State the blood parasite species.
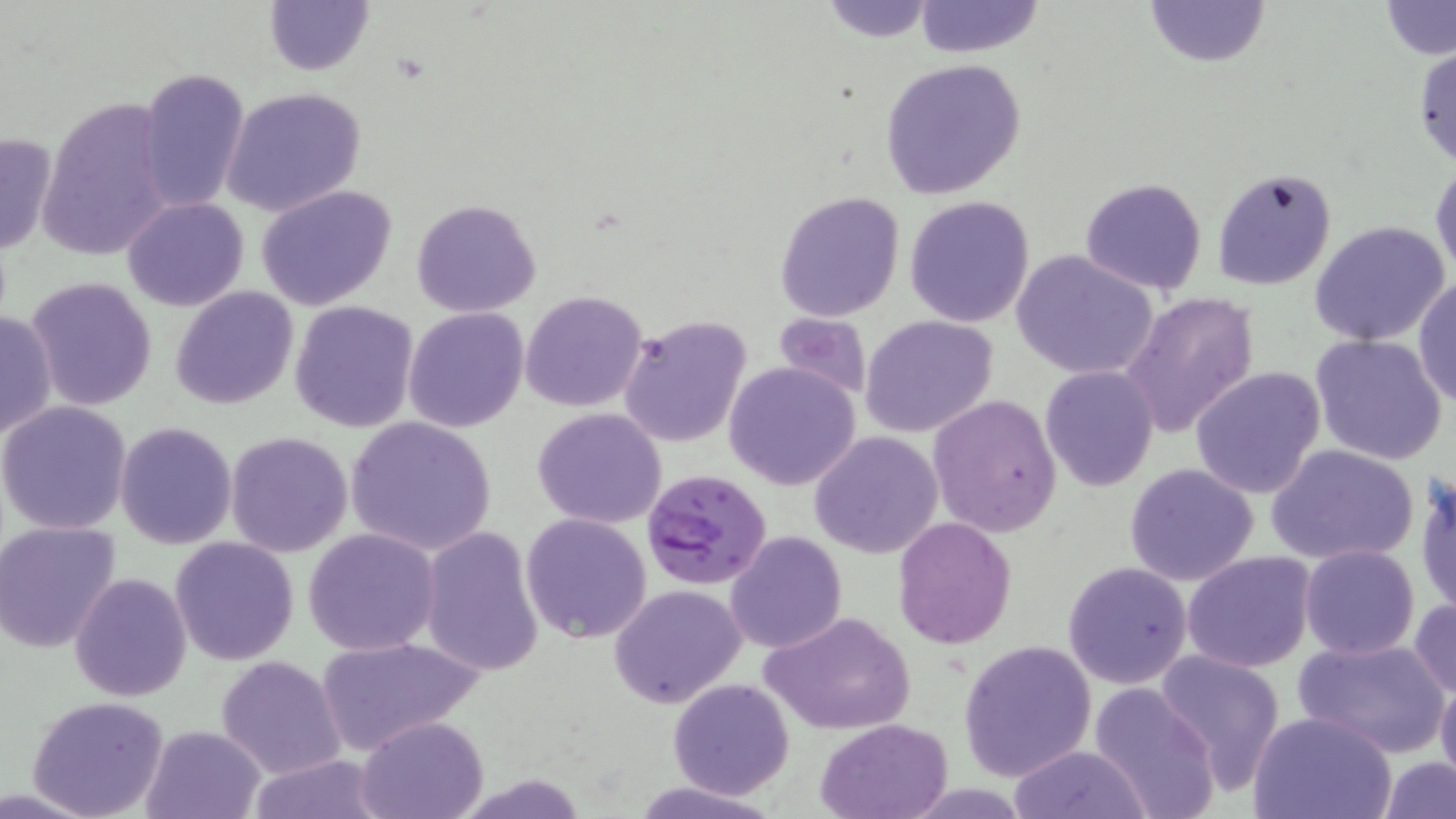

Plasmodium falciparum.

{
  "magnification": "1000x",
  "plasmodium_falciparum_infected_red_blood_cell_locations": "approximate bounding boxes as named x1/y1/x2/y2 corners in pixels: (x1=643, y1=469, x2=772, y2=591)",
  "stain": "May-Grünwald-Giemsa",
  "image_size": "1456×819 pixels",
  "modality": "optical microscopy",
  "preparation": "thin blood film",
  "field_of_view": "single",
  "uninfected_red_blood_cell_locations": "approximate bounding boxes as named x1/y1/x2/y2 corners in pixels: (x1=262, y1=0, x2=374, y2=77), (x1=818, y1=0, x2=938, y2=43), (x1=1139, y1=0, x2=1273, y2=69), (x1=912, y1=1, x2=1045, y2=57), (x1=1378, y1=1, x2=1456, y2=58), (x1=1412, y1=42, x2=1456, y2=168), (x1=879, y1=58, x2=1027, y2=199), (x1=136, y1=66, x2=251, y2=215), (x1=221, y1=86, x2=366, y2=217), (x1=34, y1=93, x2=176, y2=263), (x1=0, y1=131, x2=57, y2=259), (x1=1430, y1=160, x2=1455, y2=282), (x1=1211, y1=165, x2=1336, y2=291), (x1=1079, y1=176, x2=1207, y2=295), (x1=255, y1=185, x2=399, y2=310), (x1=773, y1=189, x2=906, y2=323), (x1=903, y1=195, x2=1035, y2=327), (x1=123, y1=197, x2=248, y2=312), (x1=411, y1=198, x2=543, y2=317), (x1=1309, y1=221, x2=1451, y2=347), (x1=1011, y1=250, x2=1158, y2=381), (x1=1414, y1=275, x2=1455, y2=409), (x1=27, y1=276, x2=160, y2=412), (x1=171, y1=285, x2=298, y2=409), (x1=520, y1=289, x2=649, y2=412), (x1=1121, y1=291, x2=1261, y2=437), (x1=289, y1=301, x2=420, y2=432), (x1=404, y1=307, x2=529, y2=432), (x1=0, y1=310, x2=55, y2=441), (x1=773, y1=312, x2=871, y2=401), (x1=859, y1=315, x2=998, y2=437), (x1=618, y1=316, x2=751, y2=447), (x1=1309, y1=333, x2=1448, y2=466), (x1=723, y1=361, x2=861, y2=490), (x1=1040, y1=365, x2=1159, y2=493), (x1=1190, y1=366, x2=1328, y2=500), (x1=927, y1=394, x2=1061, y2=539), (x1=0, y1=402, x2=133, y2=535), (x1=532, y1=407, x2=668, y2=529), (x1=345, y1=415, x2=496, y2=557), (x1=115, y1=421, x2=238, y2=550), (x1=810, y1=430, x2=944, y2=558), (x1=224, y1=431, x2=353, y2=558), (x1=1266, y1=443, x2=1420, y2=567), (x1=1124, y1=463, x2=1258, y2=587), (x1=1416, y1=476, x2=1456, y2=617), (x1=520, y1=512, x2=653, y2=644), (x1=893, y1=518, x2=1017, y2=648), (x1=0, y1=521, x2=121, y2=652), (x1=302, y1=527, x2=442, y2=656), (x1=419, y1=528, x2=544, y2=677), (x1=725, y1=530, x2=847, y2=654), (x1=171, y1=536, x2=298, y2=665), (x1=1299, y1=543, x2=1419, y2=659), (x1=1182, y1=551, x2=1316, y2=674), (x1=1065, y1=562, x2=1193, y2=689), (x1=69, y1=571, x2=193, y2=703), (x1=608, y1=583, x2=748, y2=709), (x1=1409, y1=597, x2=1456, y2=699), (x1=760, y1=608, x2=917, y2=735), (x1=314, y1=634, x2=481, y2=756), (x1=1294, y1=635, x2=1449, y2=756), (x1=958, y1=638, x2=1097, y2=780), (x1=1155, y1=650, x2=1286, y2=793), (x1=216, y1=653, x2=346, y2=778), (x1=1436, y1=677, x2=1456, y2=790), (x1=667, y1=678, x2=796, y2=799), (x1=1087, y1=681, x2=1220, y2=819), (x1=26, y1=695, x2=171, y2=819), (x1=1250, y1=711, x2=1396, y2=819), (x1=356, y1=716, x2=488, y2=819), (x1=815, y1=718, x2=955, y2=818), (x1=140, y1=725, x2=266, y2=819), (x1=1009, y1=744, x2=1150, y2=819), (x1=242, y1=756, x2=392, y2=818), (x1=1378, y1=757, x2=1456, y2=818), (x1=631, y1=779, x2=778, y2=819)"
}